Give the position of every malaria parasite.
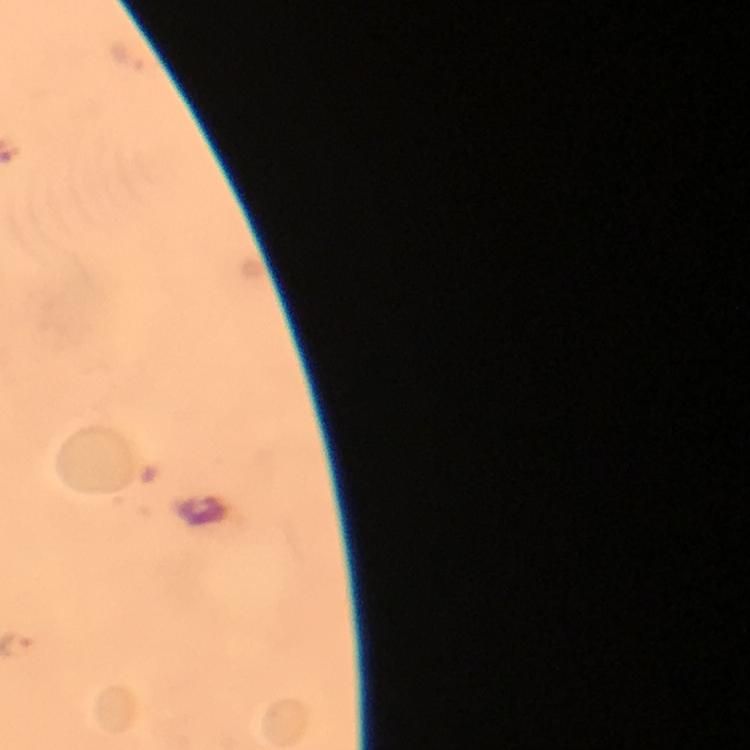
Approximate centers as {x, y} in pixels.
Malaria parasites: {128, 58}.

From a malaria diagnostic workup. Immersion oil applied. Photographed with a smartphone mounted on the microscope. Image is 750×750 pixels. At 100x magnification. Cropped region of a single field of view. Giemsa-stained preparation. Thick blood film.